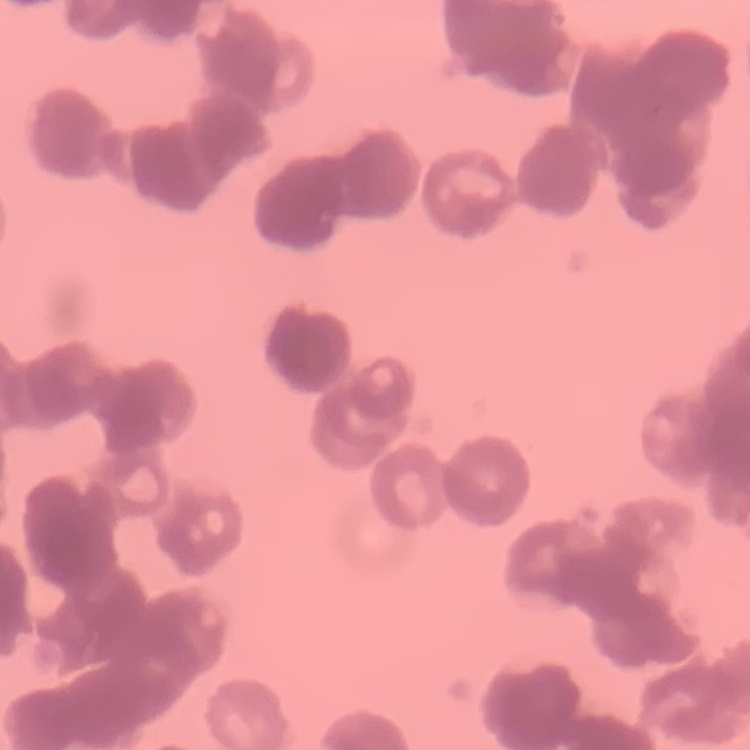

red_blood_cell_morphology: rouleaux formation
preparation: thin blood smear
stain: Field's or Giemsa
image_type: one tile cut from a larger photomicrograph